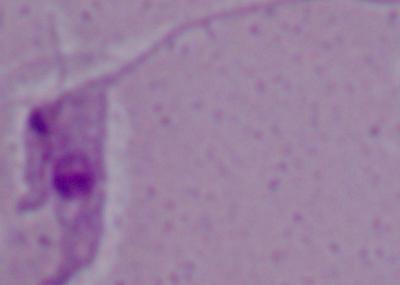
Summary:
  - Magnification: 1000x
  - Modality: photomicrograph
  - Identification: Leishmania